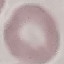
{
  "result": "no malaria parasites seen",
  "image_type": "automatically extracted cell patch, resized to 64 × 64 pixels",
  "capture": "smartphone through the microscope eyepiece",
  "preparation": "thin blood smear",
  "stain": "Giemsa"
}